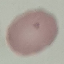

Result: no malaria parasites detected. Automatically extracted cell patch, resized to 64 × 64 pixels. Giemsa stain. Photographed with a smartphone camera at the microscope eyepiece. Thin blood film.